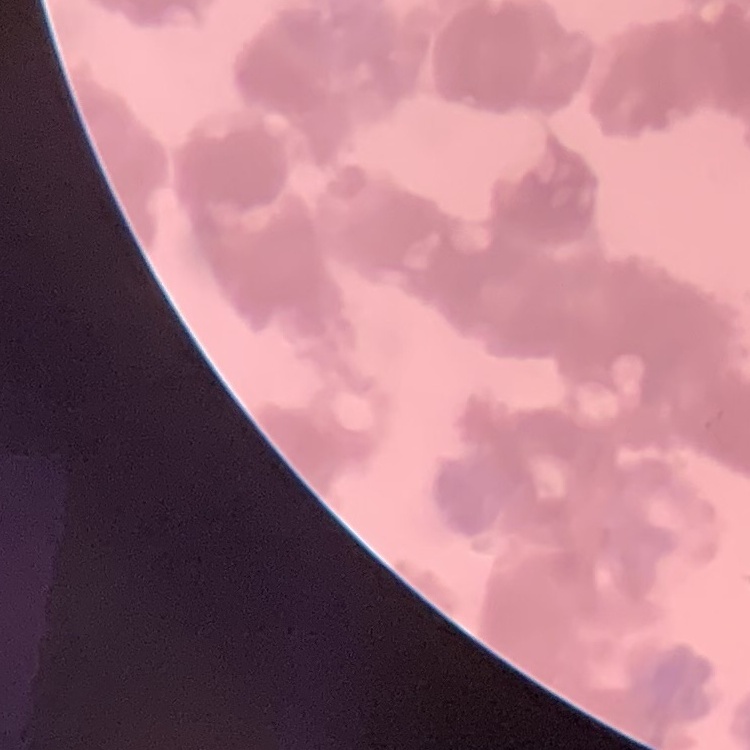
red_blood_cell_morphology: rouleaux formation
preparation: thin blood film
stain: Field's or Giemsa
image_type: one tile cut from a larger photomicrograph